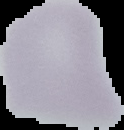

Summary:
  - Image size: 124×130 pixels
  - Result: no malaria parasites seen
  - Image type: segmented cell region on a black background
  - Preparation: thin blood smear